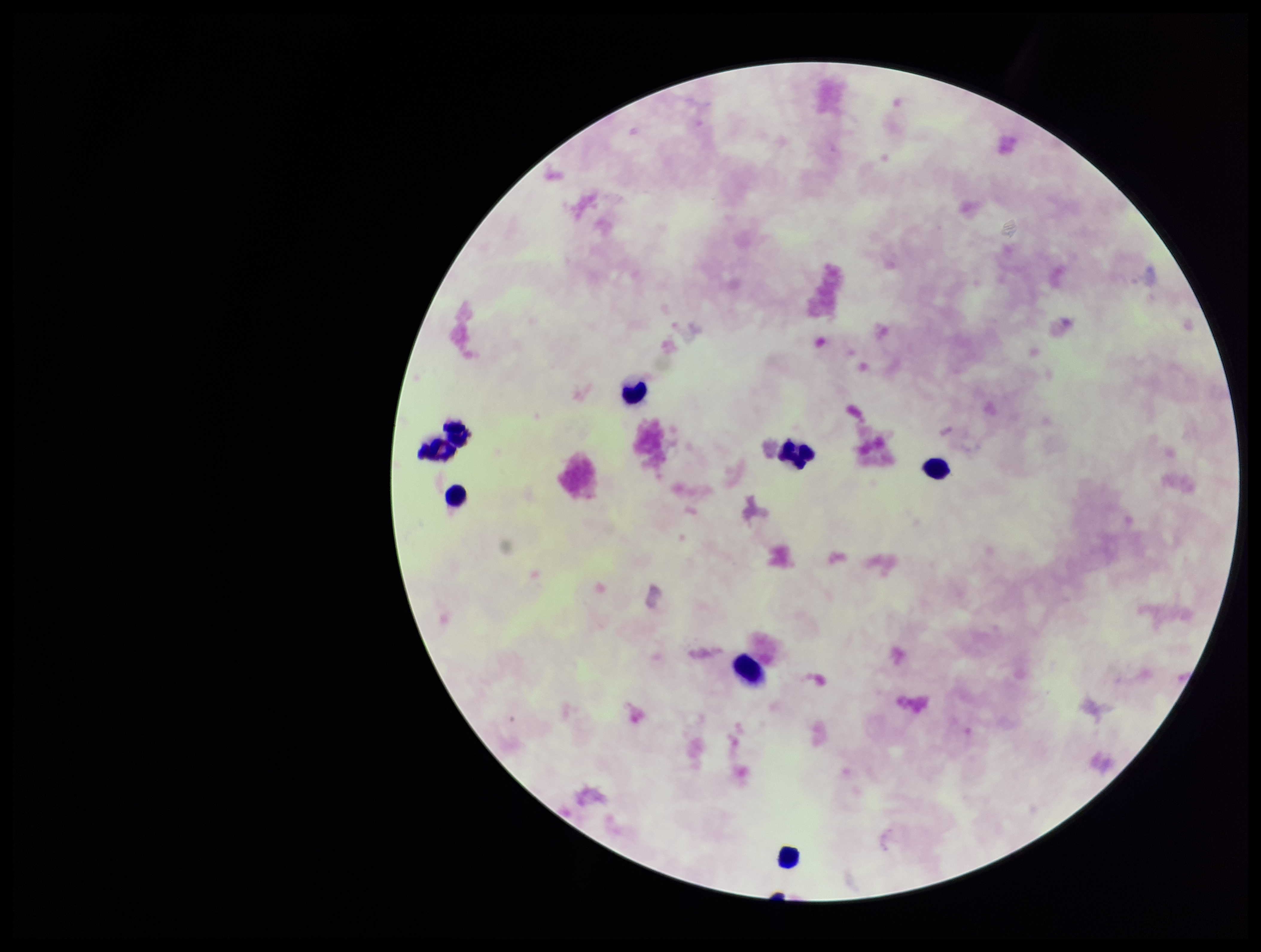 Single field of view. Patient malaria status: negative. Preparation: thick smear. Parasite count: 0. Giemsa stain. Leukocyte count: 8. Image is 1261×952 pixels. Plasmodium parasites: none identified. Smartphone photograph taken through the eyepiece of a microscope.